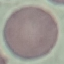
Summary:
  - Result: negative for malaria parasites
  - Preparation: thin blood smear
  - Capture: smartphone through the microscope eyepiece
  - Stain: Giemsa
  - Image type: automatically extracted cell patch, resized to 64 × 64 pixels